State which parasite is depicted.
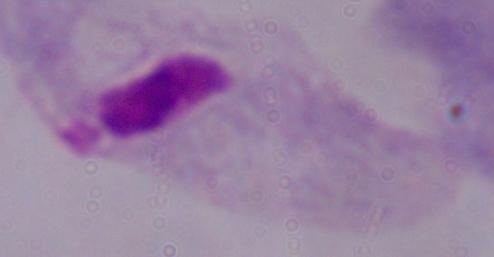
A trichomonad.

{
  "modality": "photomicrograph",
  "magnification": "1000x"
}